Assess this cell for malaria.
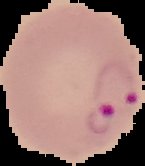

Parasitized.

preparation = thin blood film
image type = segmented cell region on a black background
image size = 145×166 pixels